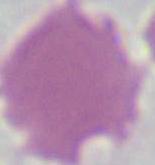

modality: photomicrograph
identification: red blood cell
magnification: 1000x